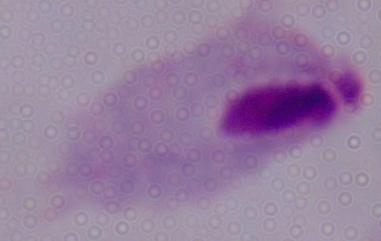
Photomicrograph. A trichomonad is shown. 1000x magnification.